Classify this cell by malaria status.
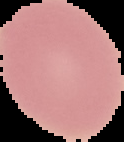
It is uninfected.

Image is 124×142 pixels. Cell region segmented out of the field of view; the surrounding area is masked to black. From a thin blood film.